Name the blood parasite species.
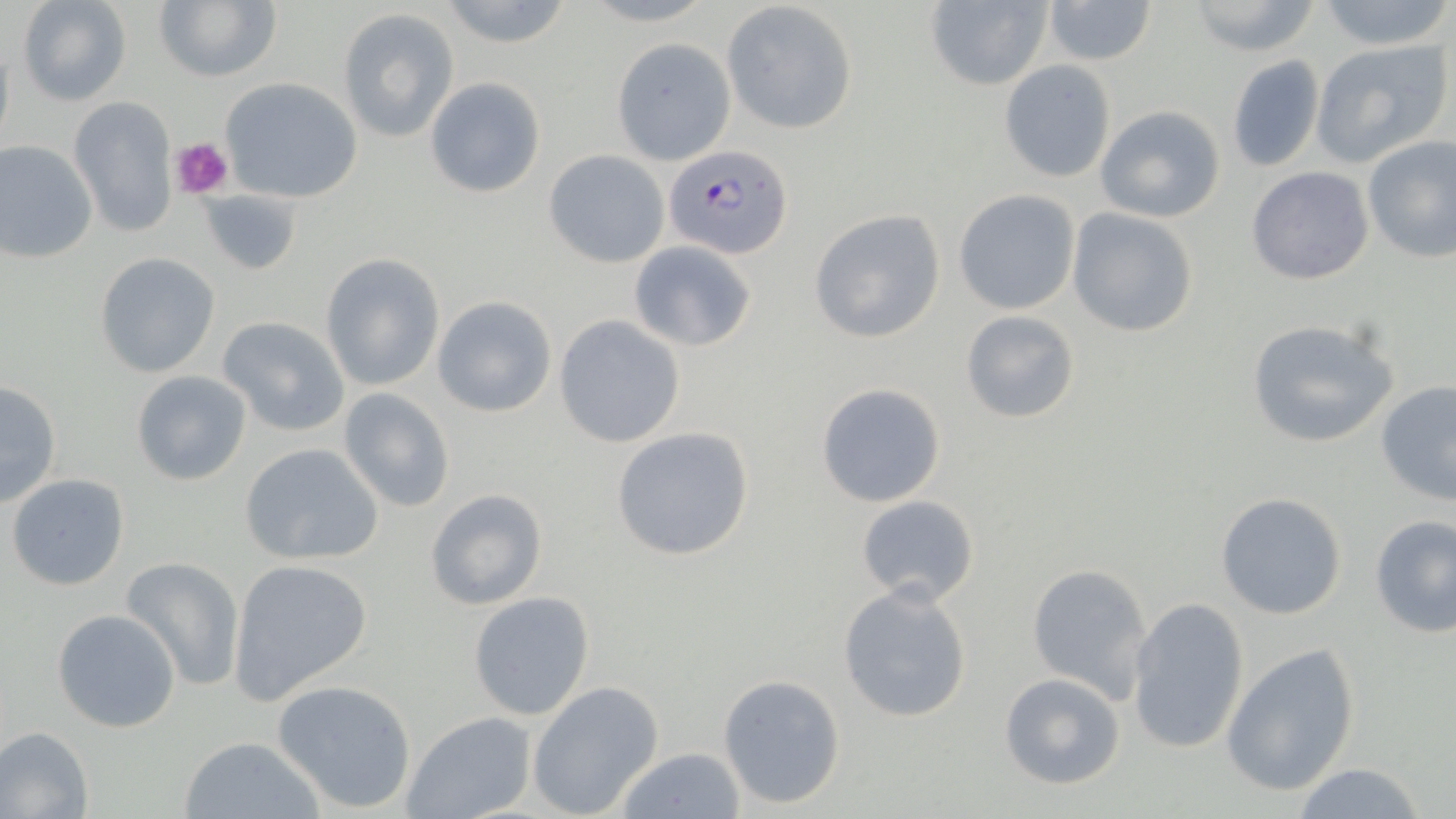

Plasmodium falciparum.

field of view = single
stain = May-Grünwald-Giemsa
image size = 1456×819 pixels
preparation = thin blood smear
magnification = 1000x
Plasmodium falciparum-infected red blood cell locations = approximate bounding boxes as [x1, y1, x2, y2] in pixels: [664, 144, 792, 259]
platelet locations = approximate bounding boxes as [x1, y1, x2, y2] in pixels: [171, 136, 235, 201]
uninfected red blood cell locations = approximate bounding boxes as [x1, y1, x2, y2] in pixels: [16, 0, 132, 107], [154, 0, 280, 83], [437, 0, 574, 49], [1041, 0, 1157, 66], [1183, 0, 1324, 58], [1312, 0, 1454, 50], [921, 1, 1052, 92], [723, 2, 859, 134], [336, 7, 460, 143], [1, 38, 15, 157], [612, 39, 735, 165], [1310, 40, 1450, 167], [1225, 53, 1326, 173], [999, 61, 1117, 183], [426, 76, 545, 198], [219, 77, 363, 203], [69, 96, 178, 237], [1094, 105, 1226, 223], [1362, 136, 1456, 263], [0, 140, 97, 264], [544, 151, 669, 268], [1245, 165, 1375, 286], [195, 189, 300, 273], [953, 189, 1081, 315], [1066, 208, 1200, 338], [809, 209, 946, 343], [629, 241, 756, 351], [94, 253, 221, 377], [321, 254, 444, 391], [432, 296, 556, 418], [959, 309, 1081, 425], [216, 315, 352, 437], [555, 315, 685, 448], [1244, 318, 1398, 450], [131, 371, 252, 487], [0, 380, 61, 506], [1376, 381, 1456, 508], [815, 383, 946, 507], [337, 389, 457, 512], [611, 426, 753, 562], [239, 442, 383, 565], [6, 472, 131, 591], [425, 489, 548, 610], [1214, 491, 1348, 620], [855, 494, 979, 606], [1368, 514, 1456, 638], [120, 556, 247, 692], [227, 558, 373, 702], [1026, 563, 1154, 703], [838, 585, 974, 724], [468, 592, 596, 722], [1127, 596, 1251, 755], [52, 608, 181, 734], [1221, 641, 1361, 801], [998, 672, 1128, 790], [719, 673, 846, 809], [273, 679, 417, 813], [526, 681, 664, 817], [402, 712, 535, 819], [0, 726, 95, 818], [178, 734, 324, 819], [615, 747, 745, 818], [1290, 762, 1430, 819]
modality = optical microscopy